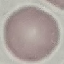 Result: no malaria parasites detected. Photographed with a smartphone camera at the microscope eyepiece. Automatically extracted cell patch, resized to 64 × 64 pixels. Giemsa-stained preparation. Thin blood smear.